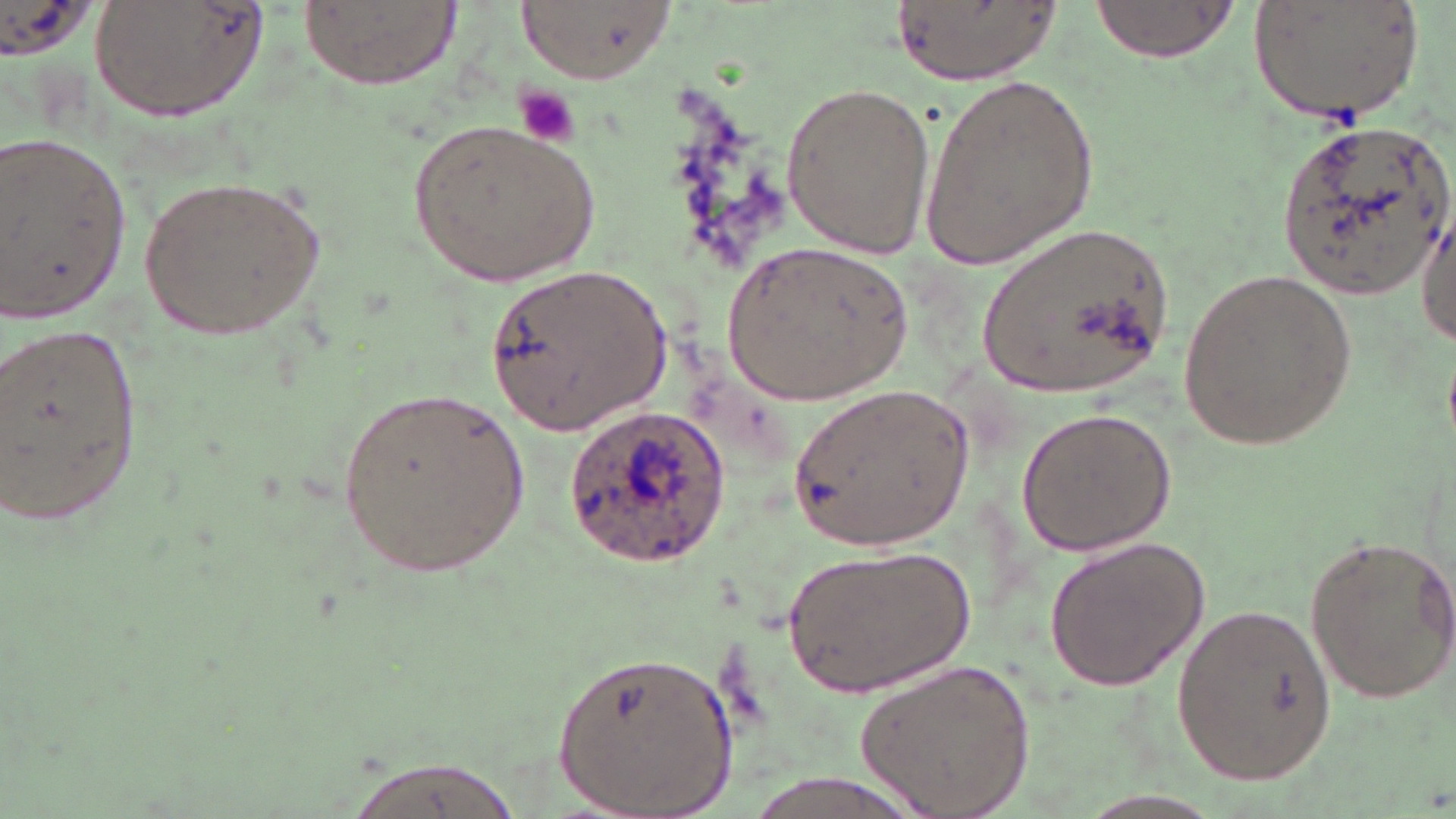
Approximate bounding boxes as [x1, y1, x2, y2] in pixels. Uninfected red blood cell locations: [89, 0, 267, 123], [300, 0, 456, 90], [524, 0, 672, 79], [894, 0, 1058, 86], [1252, 0, 1422, 126], [1088, 1, 1234, 61], [919, 69, 1100, 270], [779, 81, 934, 259], [414, 116, 603, 285], [1278, 116, 1452, 296], [0, 127, 136, 325], [141, 173, 328, 340], [1416, 215, 1455, 349], [974, 227, 1175, 404], [719, 243, 916, 407], [484, 264, 669, 437], [1178, 266, 1358, 453], [0, 322, 146, 528], [788, 381, 976, 555], [336, 382, 531, 578], [1015, 406, 1176, 555], [1302, 531, 1456, 702], [1044, 535, 1210, 693], [783, 545, 975, 697], [1171, 598, 1338, 786], [554, 649, 739, 818], [855, 657, 1036, 819], [339, 753, 529, 819]. Platelet locations: [515, 87, 576, 147]. Plasmodium ovale-infected red blood cell locations: [565, 406, 735, 564]. Slide-level diagnosis: Plasmodium ovale. Optical microscopy. Image is 1456×819 pixels. Single field of view. May-Grünwald-Giemsa stain. 1000x magnification. Thin blood film.